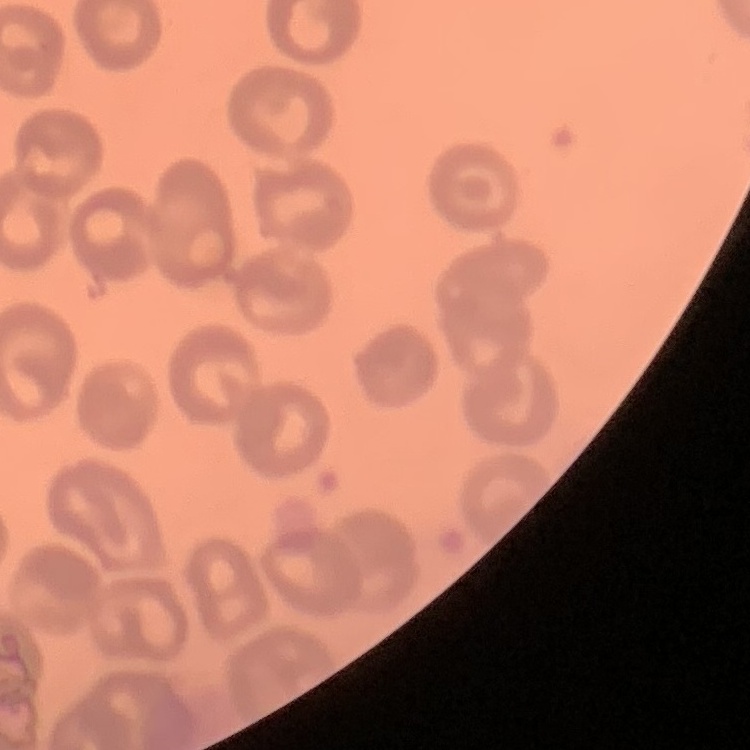
The red blood cells exhibit no rouleaux formation. Thin blood film. Field's or Giemsa stain. Square crop of a larger photomicrograph.